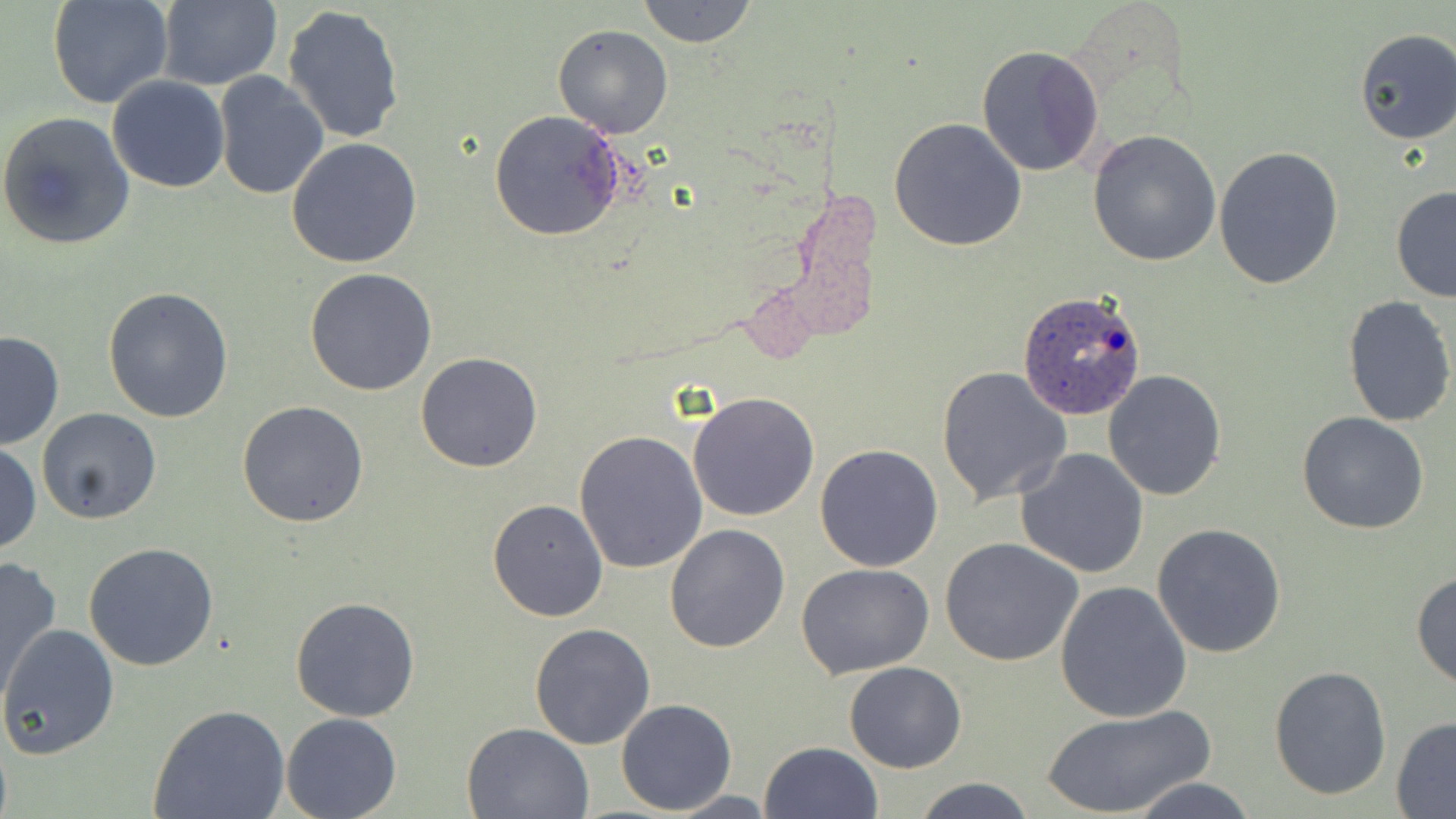
Approximate bounding boxes as (x1, y1, x2, y2) in pixels. Uninfected red blood cell locations: (47, 0, 174, 110), (156, 0, 282, 91), (636, 0, 758, 49), (283, 5, 405, 144), (552, 25, 673, 138), (1354, 28, 1456, 145), (977, 45, 1105, 178), (213, 72, 329, 200), (106, 75, 231, 193), (0, 111, 136, 252), (489, 111, 624, 242), (888, 117, 1027, 252), (1087, 129, 1223, 267), (286, 137, 423, 268), (1213, 147, 1345, 290), (1389, 184, 1456, 303), (305, 267, 438, 396), (103, 287, 234, 425), (1341, 294, 1455, 429), (0, 330, 65, 451), (415, 353, 543, 473), (937, 365, 1073, 507), (1102, 369, 1227, 501), (688, 391, 822, 522), (238, 400, 369, 527), (37, 409, 163, 527), (1297, 412, 1429, 534), (574, 431, 708, 574), (1, 442, 41, 556), (814, 444, 945, 573), (1015, 448, 1148, 578), (487, 497, 609, 621), (663, 523, 789, 652), (1152, 524, 1286, 658), (939, 538, 1084, 667), (83, 541, 219, 670), (0, 558, 64, 709), (795, 564, 934, 679), (1411, 571, 1456, 692), (1055, 581, 1191, 723), (290, 595, 420, 723), (0, 623, 120, 759), (530, 624, 656, 749), (843, 660, 967, 772), (1269, 665, 1394, 801), (614, 698, 737, 815), (149, 705, 291, 819), (1041, 705, 1214, 819), (281, 712, 401, 819), (1391, 717, 1456, 815), (464, 721, 593, 818), (760, 741, 883, 819), (1127, 776, 1257, 818), (912, 777, 1037, 818), (662, 791, 784, 818). Plasmodium ovale-infected red blood cell locations: (1017, 290, 1147, 422). Slide-level diagnosis: Plasmodium ovale. Light microscopy. May-Grünwald-Giemsa stain. 1000x magnification. One field of a larger specimen. Image is 1456×819 pixels. Thin blood film.